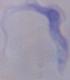

Micrograph. A trypanosome is seen. Captured at 1000x magnification.